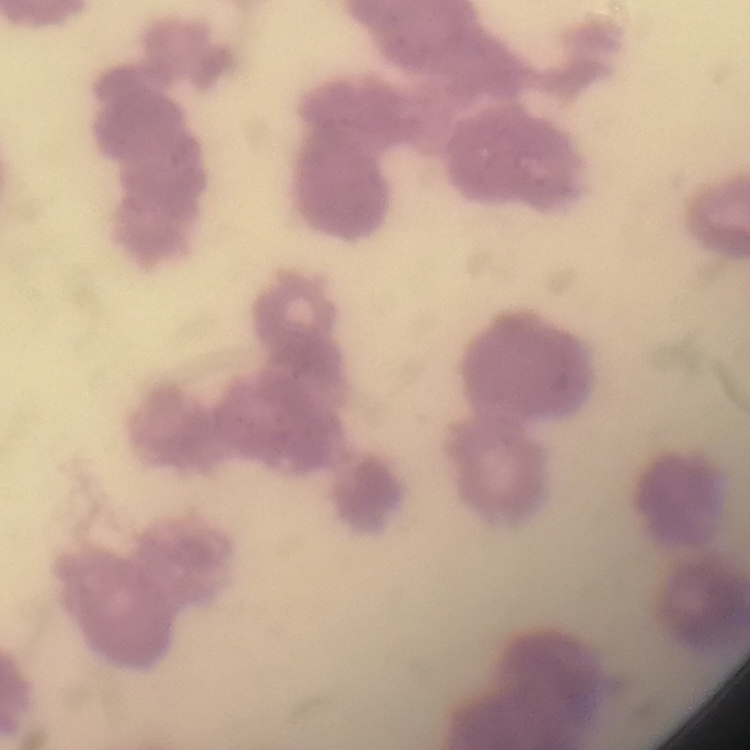 The red blood cells exhibit rouleaux formation. Stained with either Field's or Giemsa. Thin peripheral smear. One tile cut from a larger photomicrograph.